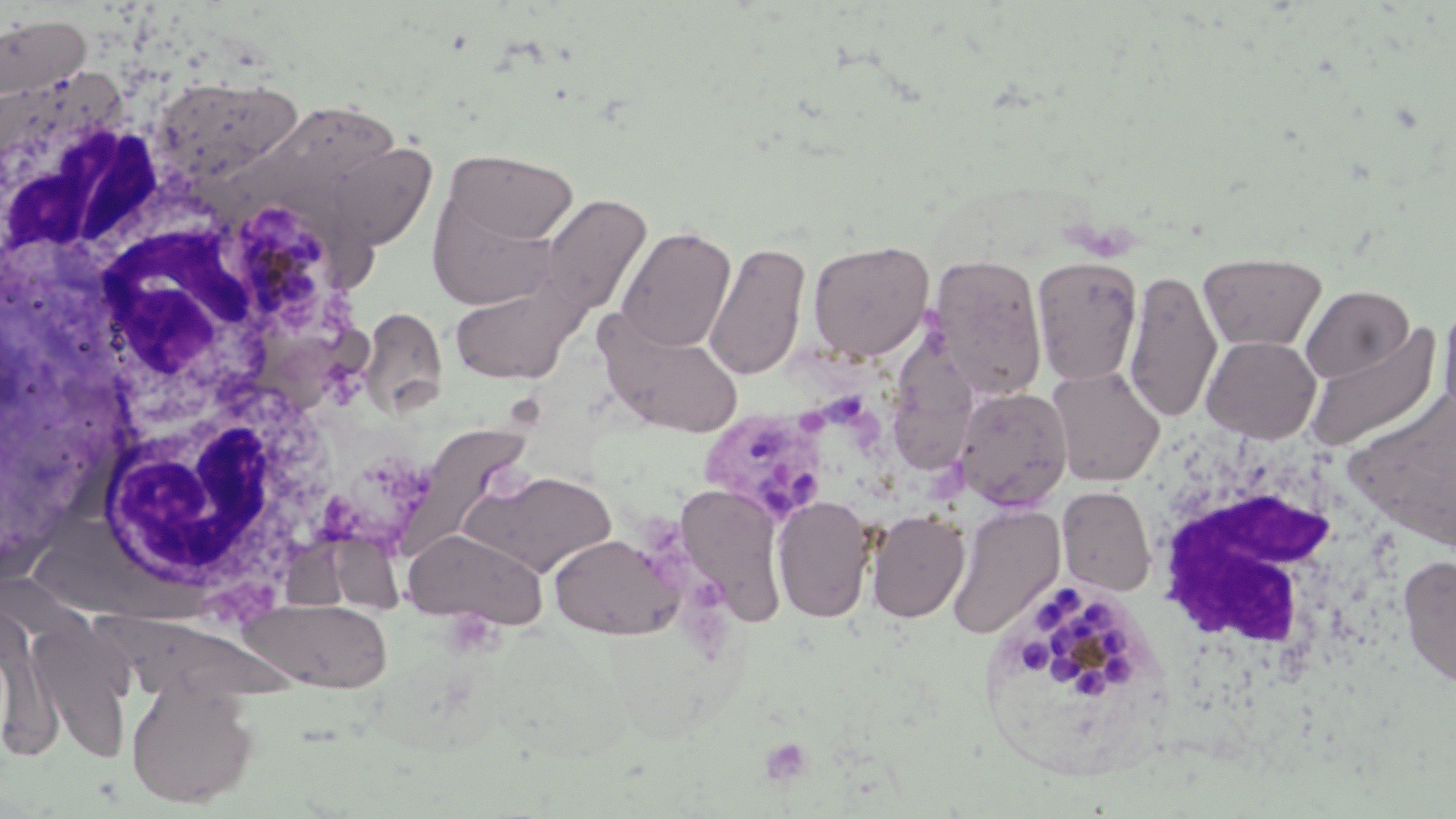
Summary:
  - Coordinate format: approximate bounding boxes as (x1, y1, x2, y2) in pixels
  - White blood cell locations: (2, 66, 190, 286), (68, 196, 256, 424), (85, 353, 341, 621), (1146, 434, 1403, 703)
  - Uninfected red blood cell locations: (0, 12, 91, 104), (151, 74, 303, 187), (227, 103, 412, 202), (338, 139, 452, 249), (444, 148, 579, 248), (426, 172, 569, 308), (539, 194, 653, 317), (616, 225, 736, 353), (807, 240, 933, 362), (703, 241, 811, 382), (1199, 251, 1327, 351), (928, 253, 1048, 399), (1031, 256, 1143, 386), (1124, 268, 1222, 423), (449, 273, 589, 386), (1301, 285, 1414, 383), (1438, 295, 1456, 422), (360, 308, 449, 417), (594, 309, 745, 437), (1303, 323, 1442, 450), (887, 329, 985, 479), (1201, 335, 1321, 441), (1046, 366, 1165, 487), (952, 386, 1073, 511), (393, 422, 536, 562), (459, 468, 617, 579), (674, 483, 787, 625), (1057, 486, 1155, 595), (773, 495, 874, 622), (948, 504, 1065, 639), (866, 509, 970, 623), (402, 528, 549, 628), (284, 534, 405, 625), (548, 534, 679, 640), (1397, 555, 1456, 688), (238, 598, 393, 692), (91, 612, 298, 706), (0, 623, 64, 760), (31, 627, 133, 766), (126, 681, 260, 808)
  - Platelet locations: (441, 608, 504, 659)
  - Plasmodium malariae-infected red blood cell locations: (235, 198, 331, 314), (699, 406, 832, 526), (1011, 576, 1138, 706)
  - Slide-level diagnosis: Plasmodium malariae
  - Field of view: one of a larger specimen
  - Magnification: 1000x
  - Preparation: thin blood film
  - Modality: optical microscopy
  - Image size: 1456×819 pixels
  - Stain: May-Grünwald-Giemsa